Identify the parasite.
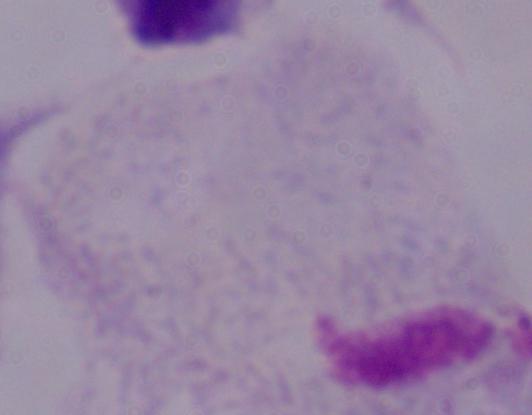

A trichomonad.

Captured at 1000x magnification. Photomicrograph.